Assess the morphology of the erythrocytes.
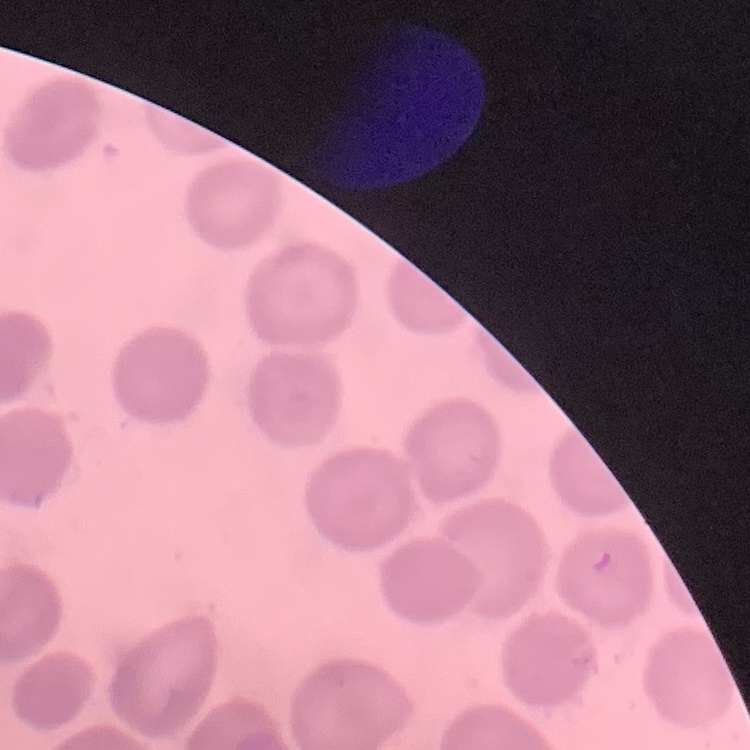

No rouleaux formation.

Summary:
  - Preparation: thin blood smear
  - Image type: square crop of a larger photomicrograph
  - Stain: Field's or Giemsa